State which cell type is depicted.
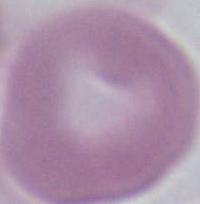
This is an erythrocyte.

Summary:
  - Modality: micrograph
  - Magnification: 1000x